Assess this cell for malaria.
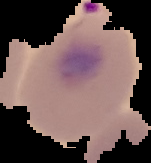
Parasitized.

Summary:
  - Image type: cell region segmented out of the field of view; surrounding area masked to black
  - Image size: 151×163 pixels
  - Preparation: thin blood smear